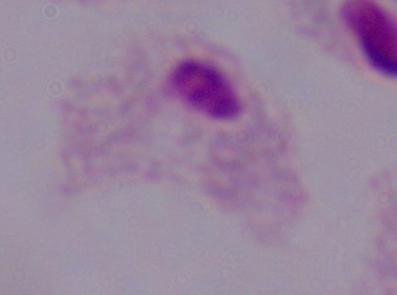

Summary:
  - Magnification: 1000x
  - Modality: micrograph
  - Identification: trichomonad